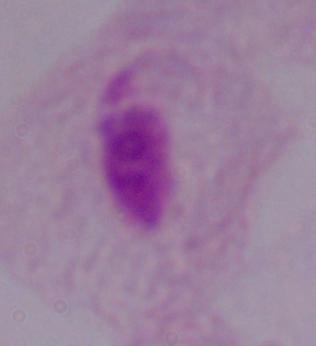

identification = trichomonad
magnification = 1000x
modality = micrograph